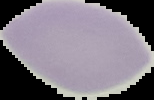

Image is 154×100 pixels. Segmented cell region on a black background. Malaria status: uninfected. From a thin blood smear.